Classify this cell by malaria status.
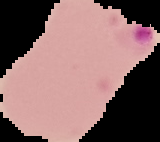
Parasitized.

Segmented cell region on a black background. Image is 160×142 pixels. From a thin blood film.